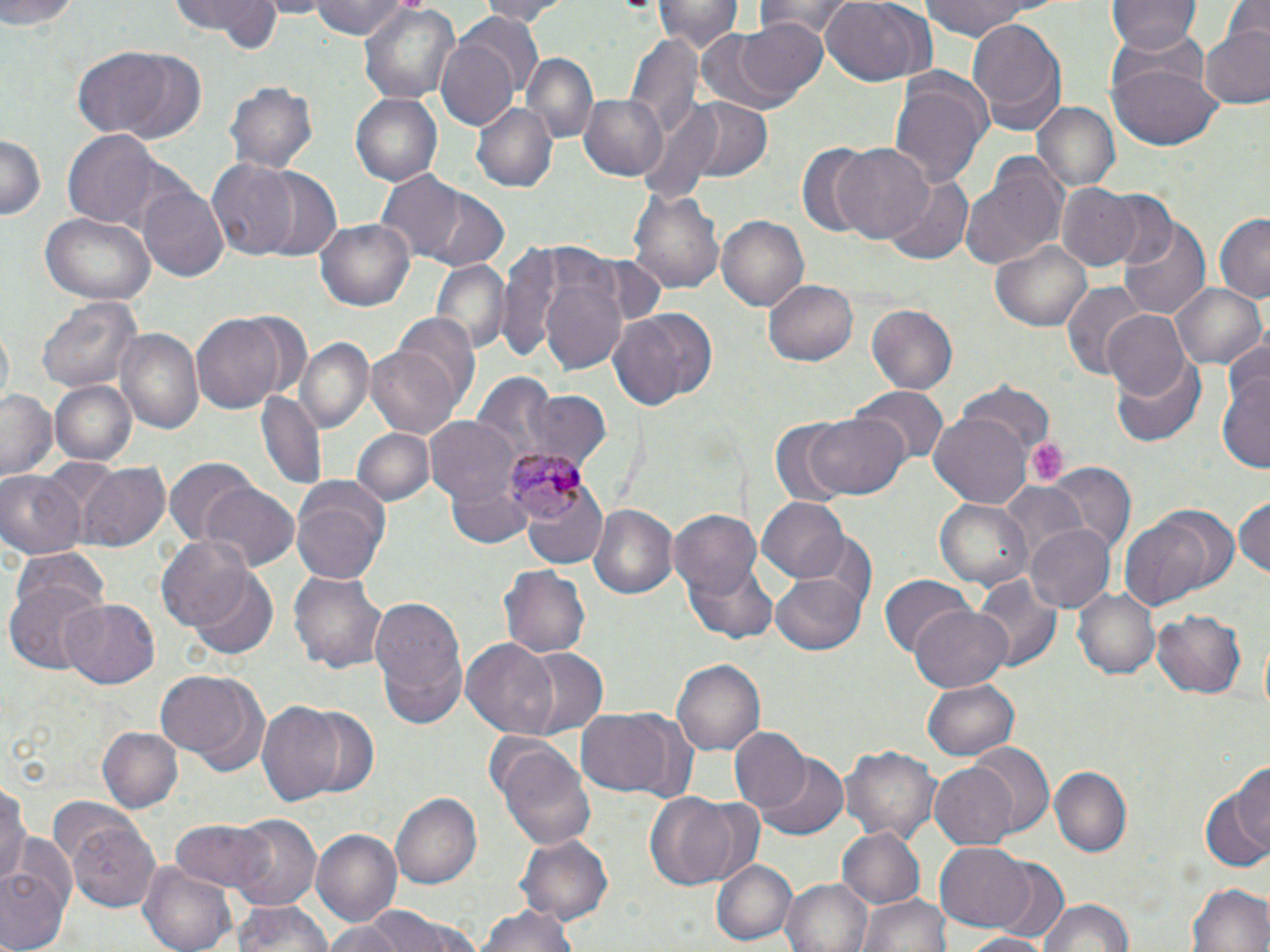
Summary:
  - Coordinate format: approximate bounding boxes as (x1, y1, x2, y2) in pixels
  - Uninfected red blood cell locations: (0, 0, 85, 27), (260, 0, 331, 16), (310, 0, 409, 41), (475, 0, 565, 24), (754, 0, 859, 40), (820, 0, 931, 87), (915, 0, 1060, 40), (1109, 0, 1200, 52), (165, 1, 285, 50), (653, 1, 739, 52), (1223, 1, 1270, 48), (360, 2, 461, 105), (457, 14, 544, 103), (966, 17, 1067, 136), (735, 18, 832, 100), (692, 26, 812, 116), (1199, 26, 1270, 109), (435, 32, 522, 134), (627, 35, 704, 138), (73, 49, 173, 135), (524, 52, 597, 143), (116, 53, 208, 144), (1109, 60, 1222, 151), (890, 72, 993, 190), (228, 81, 317, 172), (351, 92, 444, 185), (577, 92, 669, 181), (676, 98, 774, 182), (1031, 100, 1119, 194), (472, 102, 557, 193), (63, 130, 162, 228), (0, 131, 45, 220), (831, 140, 936, 243), (795, 144, 887, 240), (960, 157, 1068, 273), (207, 160, 300, 258), (249, 167, 343, 261), (372, 171, 470, 262), (882, 174, 973, 267), (1058, 183, 1146, 273), (138, 184, 230, 282), (628, 186, 725, 296), (417, 188, 512, 271), (1092, 189, 1179, 274), (1119, 211, 1210, 321), (43, 213, 156, 307), (1215, 214, 1270, 302), (717, 216, 812, 310), (317, 218, 417, 312), (990, 236, 1092, 332), (505, 241, 632, 373), (429, 261, 511, 355), (765, 279, 858, 367), (1061, 282, 1146, 381), (1171, 283, 1266, 372), (36, 294, 140, 395), (867, 304, 957, 395), (610, 309, 715, 415), (1103, 311, 1193, 404), (191, 313, 285, 414), (393, 314, 482, 410), (115, 328, 202, 433), (300, 339, 372, 431), (366, 341, 464, 439), (1112, 352, 1207, 447), (1218, 369, 1270, 475), (471, 373, 560, 471), (50, 379, 138, 467), (960, 383, 1053, 463), (853, 387, 947, 468), (1, 389, 60, 481), (521, 389, 610, 474), (257, 391, 327, 493), (929, 411, 1030, 505), (806, 413, 909, 500), (424, 417, 521, 507), (765, 422, 854, 504), (352, 427, 436, 508), (164, 459, 256, 546), (75, 462, 170, 552), (1040, 464, 1134, 551), (0, 471, 86, 561), (518, 476, 609, 570), (994, 480, 1088, 575), (291, 481, 391, 587), (202, 483, 300, 571), (445, 485, 534, 550), (1234, 492, 1269, 583), (934, 496, 1033, 590), (756, 497, 849, 584), (590, 504, 678, 600), (667, 509, 765, 597), (1120, 514, 1219, 610), (1024, 523, 1116, 613), (809, 530, 875, 611), (156, 535, 254, 632), (685, 560, 778, 644), (500, 566, 591, 660), (185, 567, 278, 659), (291, 571, 388, 673), (971, 571, 1064, 673), (878, 572, 973, 659), (772, 573, 868, 654), (6, 577, 107, 677), (1072, 586, 1161, 680), (368, 593, 468, 728), (60, 597, 162, 687), (1152, 605, 1248, 698), (908, 606, 1011, 691), (461, 639, 560, 739), (517, 648, 609, 740), (673, 659, 765, 758), (157, 670, 263, 765), (924, 677, 1019, 762), (259, 700, 346, 808), (299, 705, 376, 798), (576, 708, 673, 797), (98, 726, 182, 814), (728, 728, 811, 815), (497, 741, 598, 851), (842, 743, 940, 845), (967, 743, 1053, 836), (756, 754, 849, 839), (1229, 758, 1270, 854), (929, 761, 1021, 850), (1049, 767, 1130, 855), (0, 780, 28, 889), (1201, 780, 1270, 871), (390, 791, 482, 890), (645, 794, 741, 887), (231, 815, 322, 912), (68, 818, 162, 913), (167, 818, 278, 893), (836, 827, 927, 910), (311, 829, 402, 928), (519, 834, 613, 920), (6, 835, 78, 929), (932, 843, 1038, 931), (709, 857, 798, 947), (987, 858, 1070, 942), (140, 861, 237, 952), (0, 867, 69, 952), (783, 878, 873, 952), (1188, 883, 1268, 952), (858, 892, 951, 952), (1037, 897, 1134, 951), (232, 899, 333, 952), (338, 904, 476, 952), (474, 907, 584, 952), (959, 932, 1054, 950)
  - Platelet locations: (1026, 436, 1070, 485)
  - Plasmodium malariae-infected red blood cell locations: (505, 448, 581, 522)
  - Slide-level diagnosis: Plasmodium malariae
  - Preparation: thin blood film
  - Image size: 1270×952 pixels
  - Field of view: one of a larger specimen
  - Stain: May-Grünwald-Giemsa
  - Magnification: 1000x
  - Modality: optical microscopy